Locate and identify every blood parasite.
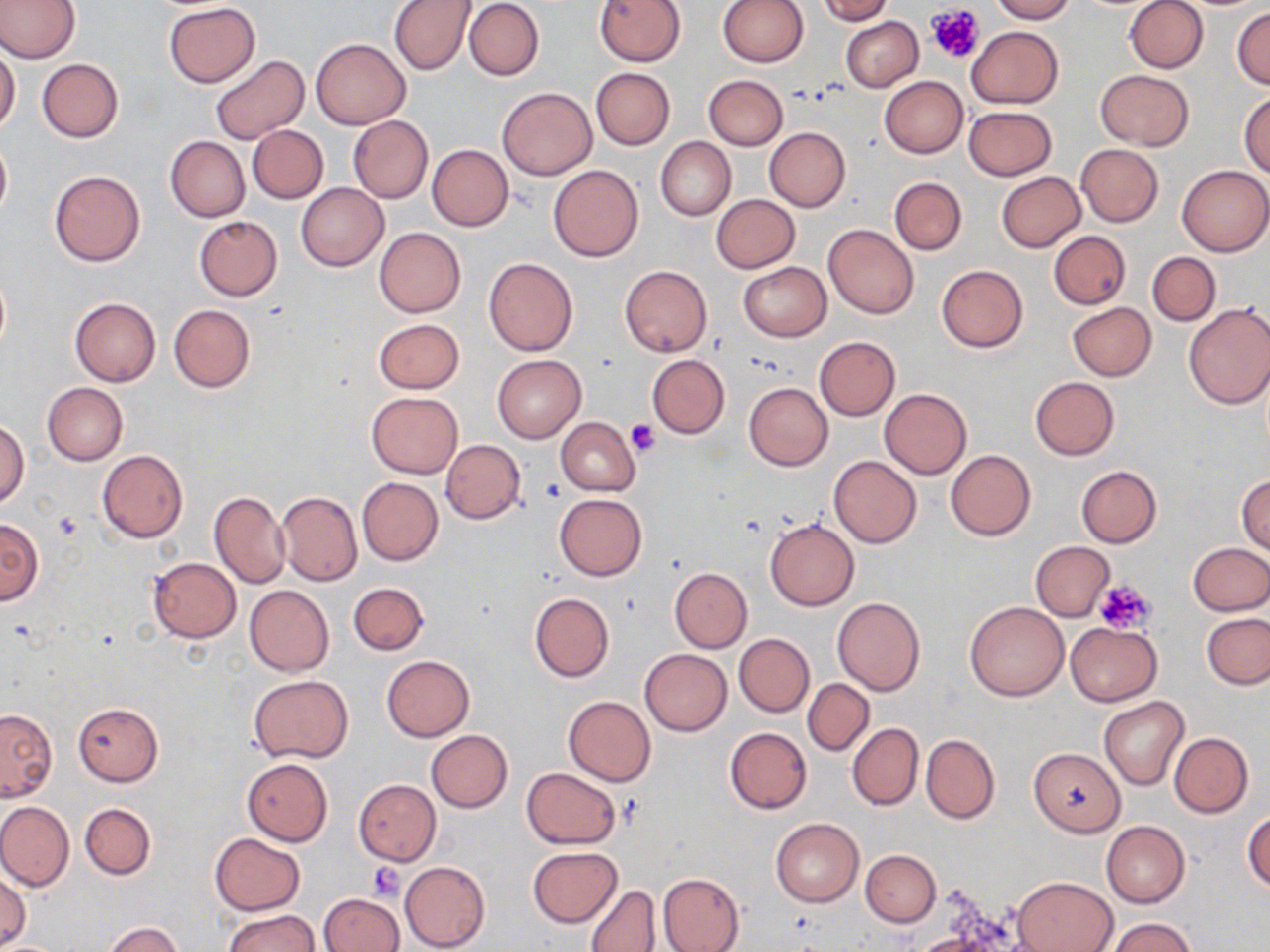

No blood parasites observed.

slide-level diagnosis = no evidence of blood parasites
field of view = single
preparation = thin blood film
uninfected red blood cell locations = approximate bounding boxes as [x1, y1, x2, y2] in pixels: [0, 0, 80, 63], [389, 0, 476, 75], [595, 0, 685, 66], [717, 0, 808, 67], [816, 0, 895, 24], [991, 0, 1075, 23], [1116, 0, 1201, 143], [1124, 0, 1208, 73], [464, 1, 544, 81], [163, 2, 259, 87], [1231, 7, 1270, 90], [841, 17, 922, 91], [966, 25, 1062, 109], [310, 38, 410, 129], [0, 44, 20, 135], [209, 54, 310, 145], [37, 58, 123, 142], [591, 68, 674, 150], [1096, 69, 1192, 149], [703, 74, 788, 150], [880, 76, 967, 158], [496, 85, 597, 180], [1239, 91, 1270, 177], [964, 106, 1057, 180], [348, 116, 433, 204], [247, 124, 329, 204], [764, 127, 850, 212], [0, 136, 12, 221], [166, 136, 249, 222], [655, 137, 735, 221], [427, 144, 514, 231], [1075, 144, 1164, 227], [547, 164, 645, 261], [1177, 164, 1270, 256], [50, 171, 146, 266], [995, 171, 1086, 252], [889, 177, 967, 255], [296, 182, 389, 271], [712, 194, 800, 272], [195, 216, 282, 300], [823, 224, 919, 319], [374, 228, 465, 317], [1048, 231, 1131, 309], [1147, 252, 1220, 325], [484, 258, 577, 356], [737, 262, 831, 342], [619, 265, 712, 357], [936, 265, 1027, 352], [0, 266, 10, 358], [69, 298, 161, 387], [1067, 302, 1156, 381], [1182, 302, 1270, 409], [168, 304, 255, 391], [373, 318, 465, 394], [814, 336, 901, 421], [646, 354, 730, 438], [492, 355, 585, 442], [1030, 376, 1120, 459], [42, 382, 127, 465], [744, 382, 834, 471], [880, 389, 972, 479], [366, 392, 462, 478], [556, 417, 640, 495], [0, 421, 30, 509], [440, 439, 525, 524], [97, 450, 189, 542], [945, 450, 1035, 540], [829, 455, 922, 548], [1075, 465, 1161, 547], [1237, 475, 1270, 555], [357, 477, 443, 565], [209, 492, 289, 590], [276, 492, 362, 586], [553, 493, 647, 580], [0, 518, 43, 606], [765, 519, 859, 611], [1030, 541, 1114, 622], [1188, 542, 1270, 616], [148, 557, 241, 642], [669, 567, 751, 652], [348, 581, 429, 656], [244, 585, 334, 676], [529, 592, 614, 683], [832, 597, 925, 696], [964, 601, 1068, 701], [1202, 613, 1270, 690], [1066, 622, 1161, 705], [733, 633, 814, 717], [640, 649, 732, 736], [382, 656, 474, 741], [249, 675, 353, 763], [803, 679, 873, 755], [563, 695, 655, 786], [1099, 696, 1188, 789], [72, 701, 162, 786], [0, 707, 57, 801], [846, 722, 923, 810], [724, 726, 811, 814], [425, 729, 513, 813], [1168, 732, 1253, 817], [921, 734, 1000, 823], [1028, 747, 1126, 836], [242, 758, 333, 846], [522, 767, 620, 849], [353, 779, 440, 864], [0, 801, 74, 891], [80, 803, 155, 879], [1243, 810, 1270, 893], [770, 816, 864, 907], [1101, 820, 1190, 908], [210, 834, 304, 915], [527, 847, 622, 928], [861, 850, 940, 926], [399, 861, 489, 950], [0, 872, 30, 949], [658, 872, 745, 952], [1014, 876, 1116, 952], [584, 884, 659, 951], [319, 893, 404, 952], [222, 909, 320, 952], [1104, 918, 1199, 952], [104, 922, 181, 952], [910, 932, 1004, 952], [0, 939, 67, 952]
image size = 1270×952 pixels
platelet locations = approximate bounding boxes as [x1, y1, x2, y2] in pixels: [925, 5, 985, 63], [626, 420, 660, 456], [54, 514, 83, 541], [1095, 579, 1154, 637], [368, 861, 405, 901]
stain = May-Grünwald-Giemsa
modality = optical microscopy
magnification = 1000x